Give the extent of all uninfected red blood cells.
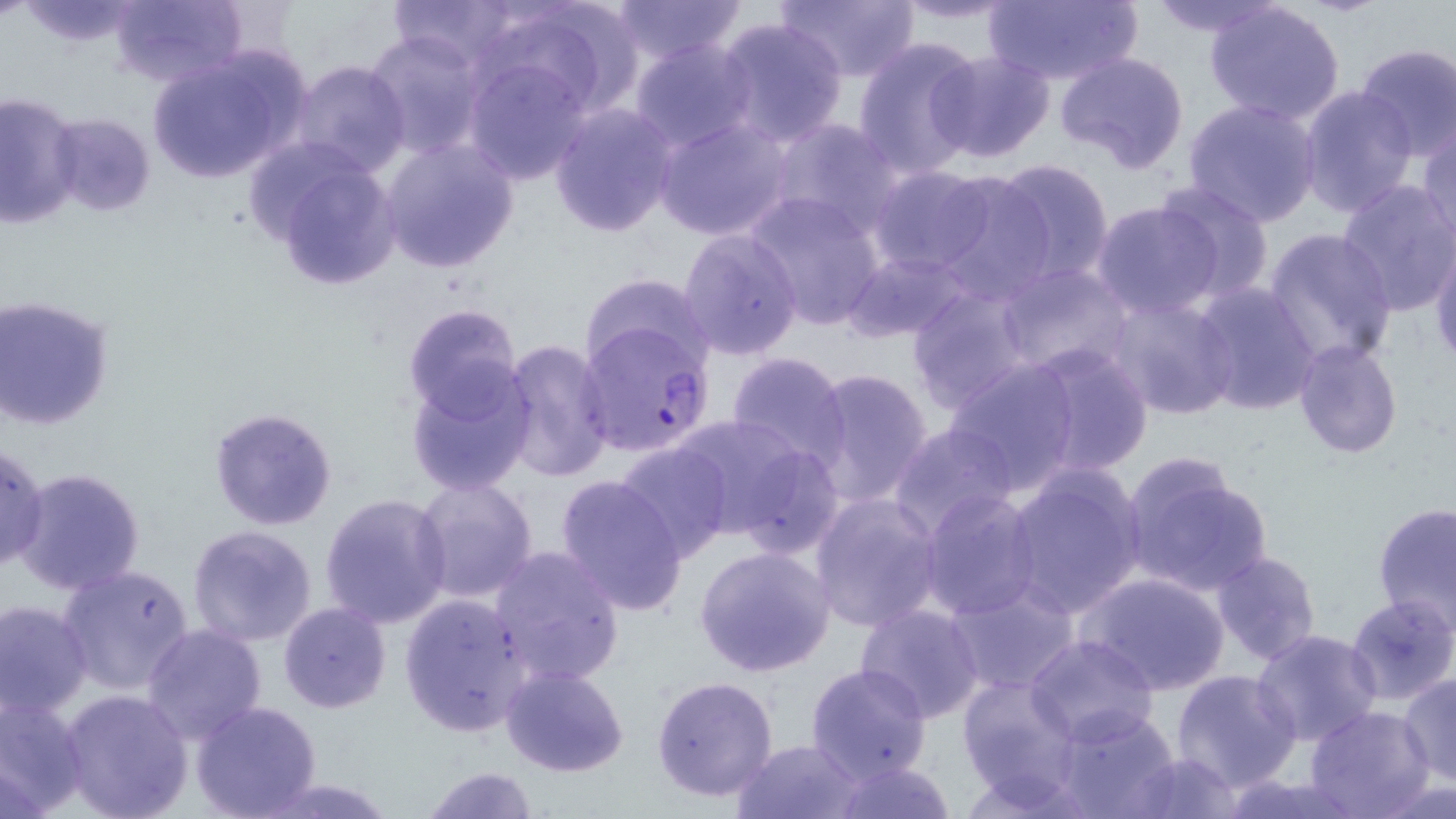

Approximate bounding boxes as (x1, y1, x2, y2) in pixels.
Uninfected red blood cells: (13, 0, 147, 48), (107, 0, 248, 89), (386, 0, 523, 71), (478, 0, 644, 123), (609, 0, 748, 64), (776, 0, 920, 81), (1144, 0, 1286, 39), (890, 1, 1028, 28), (981, 2, 1141, 85), (1204, 2, 1345, 125), (714, 16, 849, 148), (365, 31, 485, 158), (853, 37, 984, 178), (630, 39, 756, 153), (1354, 43, 1455, 162), (144, 46, 311, 187), (929, 50, 1055, 163), (1053, 52, 1191, 174), (464, 56, 592, 185), (290, 61, 410, 177), (1297, 84, 1418, 216), (0, 91, 84, 228), (1183, 98, 1323, 226), (549, 104, 679, 237), (46, 113, 157, 217), (654, 116, 793, 241), (769, 118, 903, 239), (1416, 120, 1456, 249), (379, 137, 519, 273), (249, 141, 406, 292), (989, 159, 1116, 283), (866, 165, 994, 274), (930, 168, 1056, 303), (1335, 179, 1456, 317), (1149, 180, 1277, 303), (745, 192, 886, 330), (1092, 201, 1227, 319), (677, 227, 804, 359), (1262, 230, 1398, 370), (1429, 237, 1455, 377), (842, 250, 971, 343), (996, 264, 1134, 378), (581, 271, 714, 378), (1192, 282, 1320, 415), (905, 283, 1037, 411), (1105, 296, 1241, 421), (2, 297, 118, 432), (401, 303, 523, 423), (496, 340, 617, 483), (1023, 340, 1154, 478), (1293, 340, 1403, 458), (724, 351, 852, 466), (943, 356, 1081, 493), (404, 366, 537, 495), (804, 368, 934, 510), (210, 406, 339, 531), (667, 414, 835, 551), (888, 422, 1021, 539), (614, 442, 733, 562), (0, 443, 49, 574), (1119, 453, 1274, 599), (13, 466, 147, 597), (1002, 467, 1146, 619), (554, 474, 688, 617), (412, 475, 540, 603), (918, 490, 1040, 621), (808, 492, 946, 633), (320, 493, 452, 630), (1371, 503, 1455, 632), (186, 523, 319, 648), (488, 544, 625, 687), (694, 546, 835, 676), (1209, 550, 1322, 669), (58, 564, 195, 695), (1079, 571, 1229, 697), (944, 583, 1078, 695), (399, 594, 532, 737), (1343, 595, 1456, 707), (0, 599, 92, 718), (279, 601, 391, 713), (853, 603, 987, 724), (141, 624, 268, 745), (1251, 628, 1383, 748), (1025, 634, 1159, 748), (804, 663, 933, 785), (501, 665, 630, 778), (1171, 669, 1300, 791), (1400, 673, 1456, 786), (957, 674, 1081, 805), (651, 675, 780, 802), (60, 688, 194, 819), (0, 695, 89, 816), (189, 700, 323, 819), (1053, 706, 1182, 818), (1304, 706, 1434, 818), (731, 738, 867, 819), (1124, 750, 1244, 818), (828, 757, 955, 819), (420, 766, 542, 819), (1373, 771, 1456, 818), (1216, 774, 1366, 818).

Plasmodium falciparum-infected red blood cell locations = approximate bounding boxes as (x1, y1, x2, y2) in pixels: (576, 321, 718, 460)
slide-level diagnosis = Plasmodium falciparum
modality = optical microscopy
preparation = thin blood film
field of view = one of a larger specimen
stain = May-Grünwald-Giemsa
magnification = 1000x
image size = 1456×819 pixels